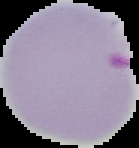
Malaria status: parasitized. Image is 139×148 pixels. Segmented cell region on a black background. From a thin blood film.